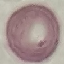
Summary:
  - Malaria status: uninfected
  - Preparation: thin blood smear
  - Image type: automatically extracted cell patch, resized to 64 × 64 pixels
  - Capture: smartphone through the microscope eyepiece
  - Stain: Giemsa